Report the malaria status of this cell.
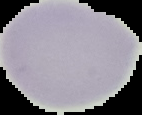

It is uninfected.

Segmented cell region on a black background. Image is 142×115 pixels. From a thin blood film.